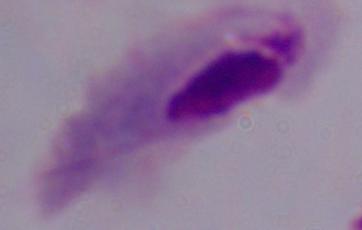

identification = trichomonad
modality = photomicrograph
magnification = 1000x